Outline each blood parasite and name the species.
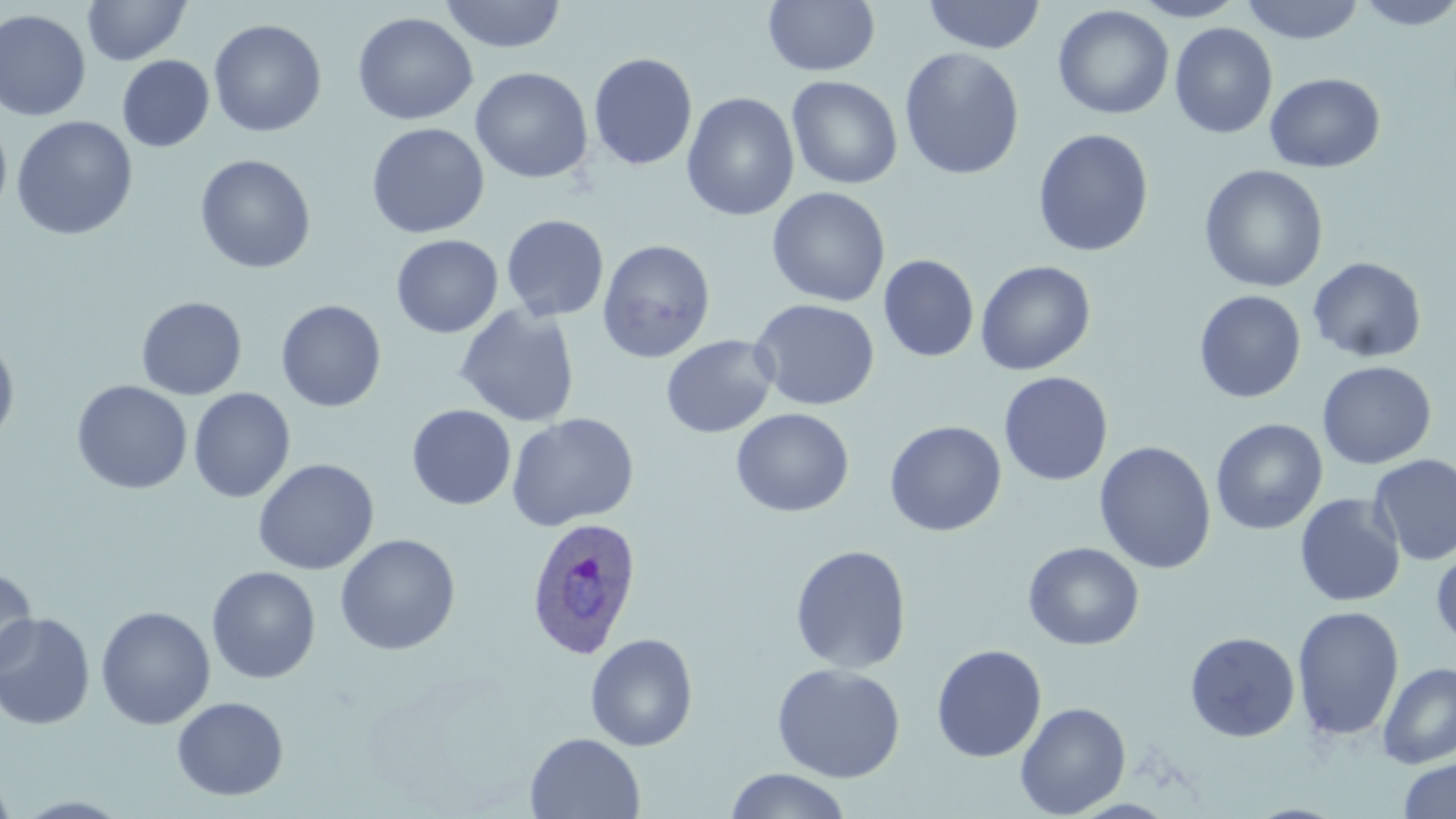
Approximate bounding boxes as (x1, y1, x2, y2) in pixels.
Plasmodium ovale-infected red blood cells: (525, 515, 644, 659).
No Plasmodium falciparum, Plasmodium malariae, Plasmodium vivax, Babesia divergens, or Trypanosoma brucei observed.

Uninfected red blood cell locations: (82, 0, 190, 66), (439, 0, 567, 53), (763, 0, 880, 76), (922, 0, 1046, 54), (1130, 0, 1247, 22), (1240, 0, 1367, 44), (1352, 0, 1456, 30), (1053, 5, 1174, 119), (0, 9, 91, 122), (352, 12, 478, 125), (208, 19, 327, 137), (1170, 22, 1277, 139), (899, 47, 1025, 180), (588, 52, 698, 171), (117, 55, 214, 152), (470, 67, 593, 184), (1265, 72, 1385, 173), (786, 75, 903, 190), (682, 92, 800, 221), (11, 115, 138, 241), (0, 118, 12, 223), (366, 122, 490, 238), (1032, 128, 1154, 257), (194, 154, 316, 274), (1199, 164, 1328, 293), (767, 187, 890, 307), (501, 214, 610, 322), (390, 234, 503, 338), (598, 239, 716, 363), (879, 255, 979, 362), (1308, 256, 1427, 363), (975, 260, 1096, 375), (990, 260, 1104, 487), (1194, 290, 1306, 403), (136, 296, 247, 400), (750, 298, 880, 411), (276, 299, 386, 413), (455, 304, 580, 427), (0, 335, 20, 449), (661, 335, 779, 438), (1317, 361, 1436, 469), (999, 371, 1113, 486), (71, 380, 193, 495), (188, 388, 295, 503), (406, 404, 516, 510), (731, 408, 854, 517), (506, 412, 640, 532), (1210, 418, 1327, 535), (884, 420, 1007, 537), (1094, 441, 1216, 574), (1369, 454, 1456, 566), (252, 458, 379, 576), (1294, 494, 1406, 608), (334, 533, 461, 655), (1023, 542, 1145, 650), (790, 544, 912, 674), (1431, 545, 1456, 649), (206, 566, 322, 684), (0, 567, 37, 676), (95, 605, 216, 729), (1292, 605, 1405, 742), (0, 611, 96, 730), (1185, 632, 1301, 743), (585, 633, 698, 751), (931, 644, 1047, 763), (771, 662, 906, 783), (1377, 662, 1456, 769), (171, 696, 289, 801), (1015, 702, 1131, 817), (525, 732, 646, 819), (1398, 757, 1456, 819), (724, 768, 853, 819), (0, 772, 17, 819). Slide-level diagnosis: Plasmodium ovale. Image is 1456×819 pixels. Thin blood film. Light microscopy. Captured at 1000x magnification. May-Grünwald-Giemsa-stained preparation. Single field of view.